Report the malaria status of this cell.
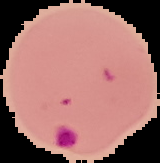

It is parasitized.

image type = cell region segmented out of the field of view; surrounding area masked to black
image size = 160×163 pixels
preparation = thin blood smear